Find each parasitized red blood cell.
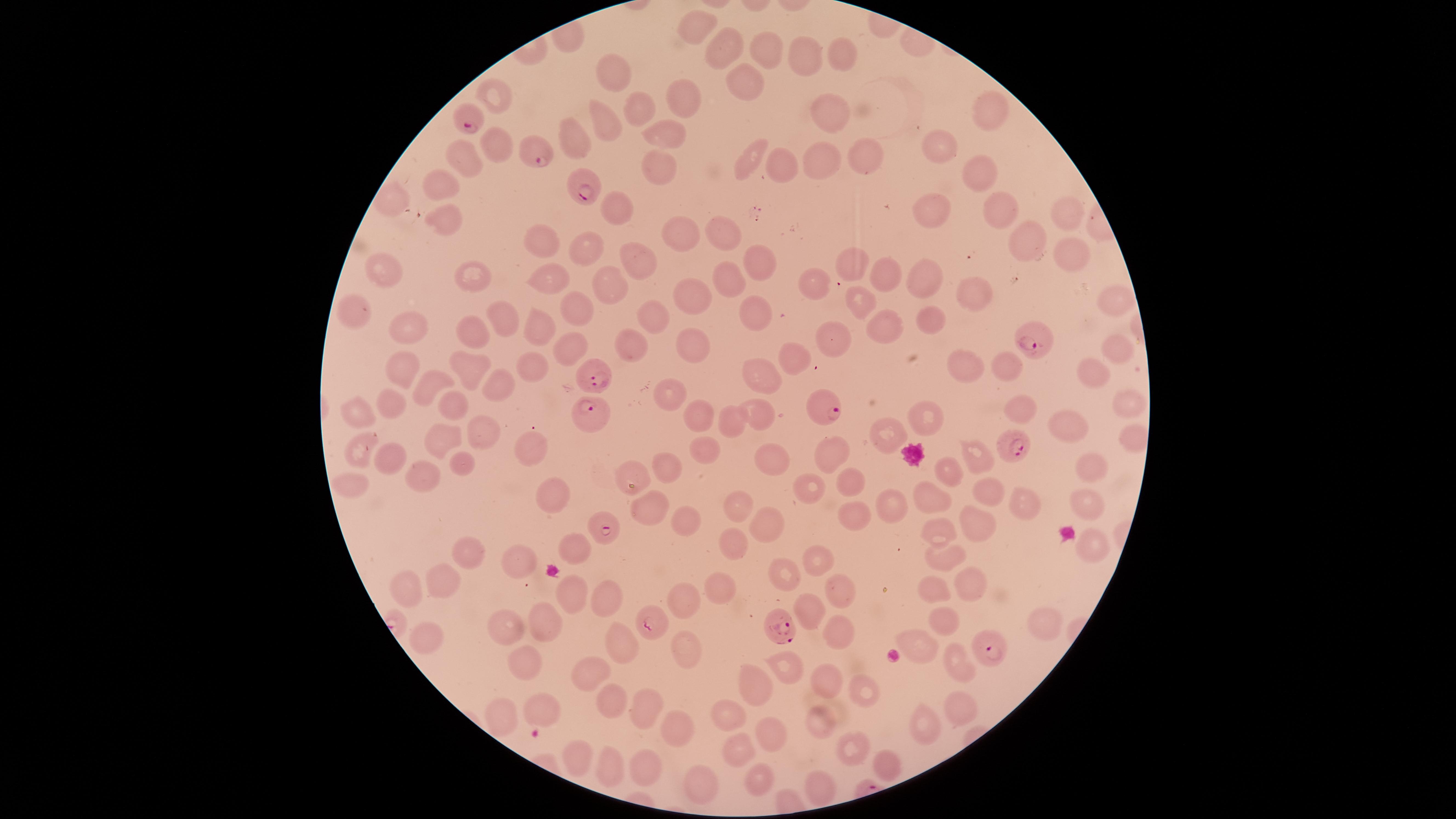

Approximate marker points, in pixels from the top-left corner.
Parasitized red blood cells: (x=465, y=125), (x=535, y=152), (x=581, y=190), (x=1035, y=335), (x=597, y=379), (x=823, y=405), (x=596, y=418), (x=1018, y=445), (x=604, y=528), (x=651, y=625), (x=781, y=628), (x=989, y=649).

Approximate marker points, in pixels from the top-left corner.
Summary:
  - Uninfected red blood cells: (x=698, y=28), (x=762, y=47), (x=723, y=48), (x=841, y=53), (x=802, y=60), (x=620, y=72), (x=744, y=85), (x=494, y=99), (x=682, y=101), (x=821, y=105), (x=637, y=110), (x=1002, y=111), (x=609, y=120), (x=576, y=135), (x=671, y=135), (x=502, y=144), (x=944, y=145), (x=756, y=151), (x=868, y=154), (x=819, y=157), (x=466, y=160), (x=660, y=166), (x=781, y=169), (x=976, y=176), (x=441, y=187), (x=933, y=207), (x=998, y=210), (x=617, y=211), (x=1068, y=214), (x=444, y=219), (x=725, y=235), (x=679, y=239), (x=1023, y=242), (x=540, y=244), (x=584, y=250), (x=1064, y=253), (x=638, y=258), (x=757, y=258), (x=850, y=258), (x=384, y=272), (x=730, y=275), (x=933, y=276), (x=820, y=277), (x=892, y=277), (x=470, y=279), (x=607, y=283), (x=547, y=284), (x=979, y=289), (x=689, y=297), (x=857, y=301), (x=1109, y=303), (x=575, y=307), (x=751, y=308), (x=651, y=313), (x=503, y=316), (x=357, y=317), (x=937, y=318), (x=407, y=326), (x=889, y=328), (x=470, y=334), (x=535, y=335), (x=833, y=341), (x=568, y=346), (x=692, y=347), (x=632, y=348), (x=1110, y=351), (x=793, y=356), (x=962, y=365), (x=1007, y=365), (x=397, y=367), (x=464, y=371), (x=530, y=372), (x=1091, y=373), (x=766, y=381), (x=430, y=383), (x=500, y=385), (x=673, y=396), (x=1124, y=397), (x=393, y=405), (x=453, y=405), (x=1021, y=408), (x=351, y=410), (x=768, y=412), (x=698, y=415), (x=921, y=422), (x=1077, y=423), (x=733, y=426), (x=487, y=431), (x=881, y=431), (x=450, y=436), (x=1135, y=441), (x=710, y=443), (x=356, y=449), (x=527, y=450), (x=983, y=450), (x=834, y=451), (x=388, y=455), (x=768, y=462), (x=671, y=465), (x=947, y=465), (x=458, y=467), (x=1085, y=468), (x=637, y=473), (x=420, y=474), (x=854, y=483), (x=807, y=485), (x=346, y=487), (x=987, y=488), (x=548, y=492), (x=929, y=493), (x=1028, y=498), (x=640, y=502), (x=1078, y=503), (x=736, y=504), (x=849, y=513), (x=889, y=513), (x=681, y=522), (x=764, y=522), (x=941, y=527), (x=969, y=528), (x=736, y=539), (x=576, y=541), (x=1084, y=547), (x=464, y=550), (x=939, y=553), (x=817, y=559), (x=521, y=563), (x=780, y=578), (x=440, y=585), (x=934, y=585), (x=962, y=585), (x=403, y=586), (x=836, y=586), (x=720, y=587), (x=572, y=593), (x=603, y=596), (x=684, y=598), (x=808, y=606), (x=542, y=618), (x=945, y=618), (x=507, y=625), (x=1053, y=627), (x=836, y=628), (x=421, y=639), (x=619, y=640), (x=920, y=642), (x=679, y=652), (x=956, y=662), (x=524, y=668), (x=778, y=668), (x=592, y=674), (x=822, y=678), (x=753, y=686), (x=863, y=690), (x=604, y=699), (x=653, y=704), (x=956, y=708), (x=538, y=711), (x=675, y=714), (x=733, y=714), (x=503, y=715), (x=915, y=725), (x=818, y=728), (x=769, y=738), (x=741, y=748), (x=850, y=749), (x=576, y=755), (x=885, y=760), (x=646, y=770), (x=607, y=775), (x=765, y=778), (x=705, y=785), (x=817, y=792)
  - Stain: Giemsa
  - Capture: smartphone photograph through the microscope eyepiece
  - Preparation: thin blood film
  - Species: Plasmodium falciparum
  - Image size: 1456×819 pixels
  - Field of view: single
  - Visible region: circular